Report the malaria status of this cell.
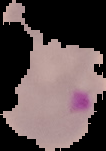
It is parasitized.

image size = 106×151 pixels
image type = segmented cell region with the area outside set to black
preparation = thin blood film